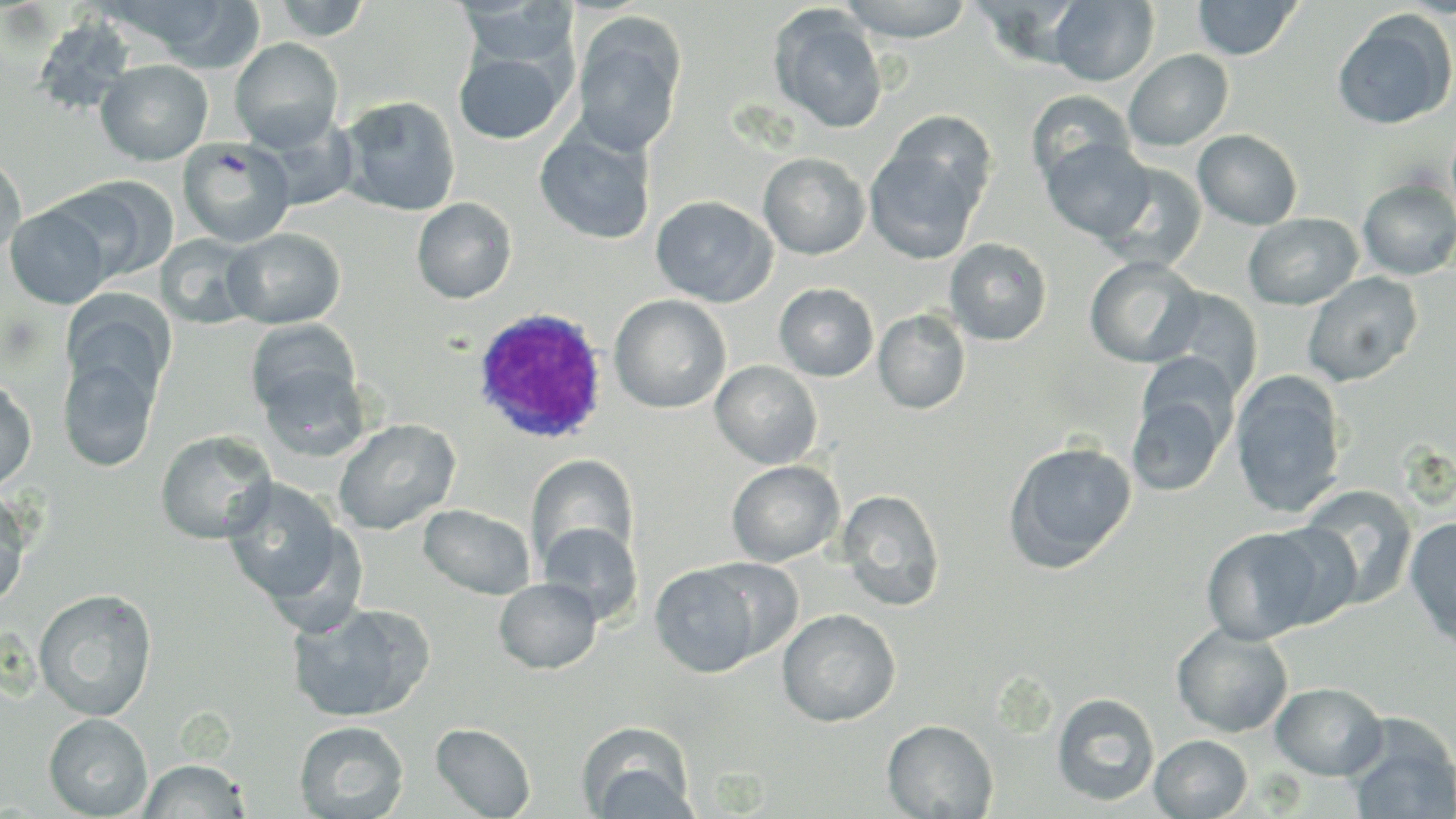
slide-level diagnosis = Plasmodium ovale
image size = 1456×819 pixels
preparation = thin blood smear
magnification = 1000x
field of view = single
uninfected red blood cell locations = approximate bounding boxes as (x1, y1, x2, y2) in pixels: (128, 0, 267, 71), (270, 0, 372, 41), (837, 0, 975, 42), (1193, 0, 1302, 60), (458, 1, 579, 71), (1048, 1, 1159, 86), (769, 5, 888, 134), (1332, 11, 1455, 129), (572, 14, 686, 157), (32, 16, 137, 117), (230, 38, 343, 150), (453, 47, 569, 145), (1124, 49, 1233, 151), (95, 59, 213, 165), (480, 66, 613, 170), (1026, 89, 1135, 189), (338, 96, 461, 217), (886, 110, 996, 219), (534, 121, 657, 246), (1193, 129, 1303, 230), (178, 138, 296, 248), (1041, 138, 1155, 242), (865, 139, 985, 264), (758, 152, 871, 259), (0, 154, 26, 262), (1095, 160, 1207, 273), (53, 177, 176, 283), (1358, 178, 1456, 280), (650, 195, 777, 307), (411, 197, 517, 304), (5, 205, 112, 309), (1242, 212, 1362, 310), (223, 227, 345, 329), (155, 234, 263, 330), (944, 238, 1052, 345), (1084, 256, 1203, 368), (1302, 272, 1423, 387), (774, 282, 879, 381), (1154, 287, 1263, 402), (62, 294, 176, 404), (610, 294, 731, 413), (873, 309, 971, 414), (245, 320, 361, 420), (58, 352, 160, 472), (710, 360, 823, 469), (256, 362, 373, 462), (1230, 371, 1347, 518), (0, 377, 37, 492), (1126, 386, 1230, 497), (332, 418, 461, 535), (155, 430, 276, 544), (1003, 440, 1138, 572), (525, 455, 638, 571), (726, 460, 844, 566), (221, 479, 351, 611), (1298, 484, 1417, 610), (0, 487, 32, 608), (837, 489, 946, 612), (418, 503, 536, 600), (1404, 516, 1456, 649), (1259, 521, 1365, 626), (538, 522, 643, 625), (1201, 526, 1329, 645), (649, 562, 766, 678), (494, 577, 602, 674), (33, 588, 157, 721), (288, 601, 435, 724), (777, 609, 900, 727), (1171, 623, 1293, 738), (1270, 681, 1388, 780), (1051, 692, 1160, 806), (43, 713, 153, 818), (882, 719, 998, 819), (294, 720, 408, 818), (1345, 720, 1456, 819), (431, 722, 536, 818), (577, 723, 698, 819), (1149, 734, 1253, 818), (138, 758, 250, 818)
modality = optical microscopy
stain = May-Grünwald-Giemsa
white blood cell locations = approximate bounding boxes as (x1, y1, x2, y2) in pixels: (472, 307, 610, 446)